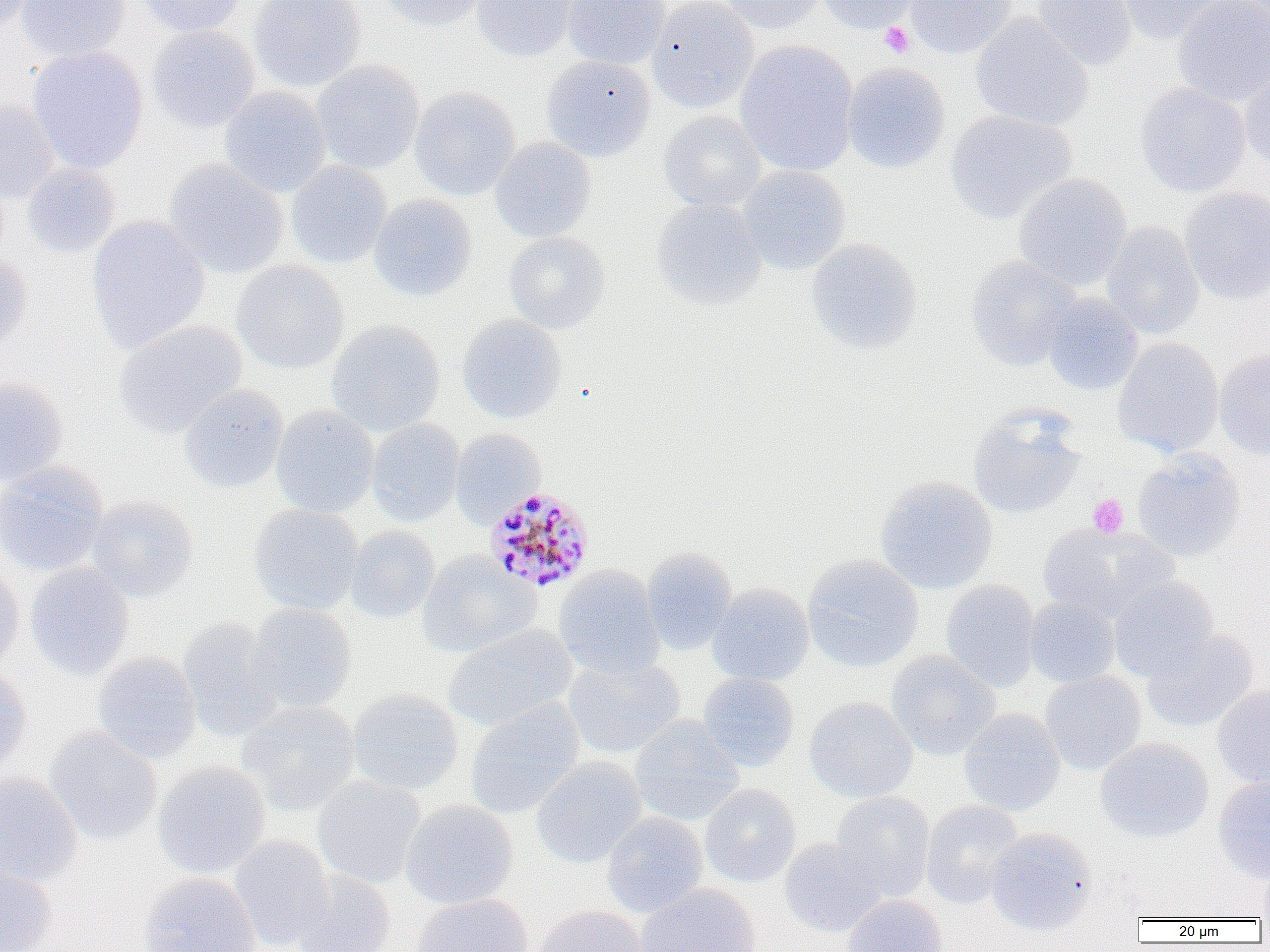
Summary:
  - Coordinate format: approximate bounding boxes as (x1,y1)-(x2,y2) corner pairs in pixels
  - Uninfected red blood cell locations: (0,0)-(34,33), (16,0)-(130,62), (133,0)-(247,37), (249,0)-(365,92), (375,0)-(487,31), (470,0)-(576,62), (562,0)-(669,70), (647,0)-(759,113), (716,0)-(826,33), (817,0)-(919,34), (905,0)-(1015,59), (1031,0)-(1136,72), (1116,0)-(1231,44), (1172,0)-(1270,105), (970,13)-(1093,132), (147,25)-(260,132), (734,40)-(858,176), (28,46)-(149,174), (542,55)-(656,162), (311,59)-(424,174), (1239,61)-(1270,170), (842,62)-(950,173), (1135,83)-(1251,198), (409,86)-(520,201), (219,87)-(331,197), (0,100)-(59,203), (945,110)-(1077,224), (658,111)-(766,212), (490,137)-(596,243), (164,159)-(289,278), (287,161)-(392,268), (22,164)-(119,258), (738,165)-(851,275), (1012,173)-(1132,291), (1179,186)-(1270,305), (369,194)-(478,303), (651,199)-(766,310), (86,215)-(209,354), (1101,222)-(1204,340), (504,232)-(610,334), (806,239)-(923,355), (0,249)-(32,355), (964,255)-(1082,372), (232,260)-(350,375), (1041,292)-(1144,395), (458,314)-(567,424), (113,320)-(248,438), (326,320)-(445,436), (1113,337)-(1224,458), (1213,348)-(1270,460), (0,377)-(68,486), (178,384)-(289,493), (271,406)-(379,518), (967,406)-(1086,520), (367,418)-(464,526), (450,429)-(547,526), (1132,448)-(1246,561), (0,461)-(108,577), (875,475)-(998,594), (86,495)-(199,602), (248,505)-(364,614), (1038,521)-(1173,622), (345,526)-(440,623), (641,547)-(738,655), (417,550)-(541,658), (802,553)-(923,673), (25,563)-(134,680), (0,565)-(24,675), (553,565)-(665,678), (1108,577)-(1219,680), (940,580)-(1040,693), (708,583)-(814,687), (1025,597)-(1120,688), (246,603)-(357,713), (177,616)-(285,742), (443,625)-(577,731), (1141,630)-(1258,733), (886,650)-(1001,760), (91,651)-(201,763), (562,655)-(684,760), (0,664)-(32,776), (1040,671)-(1146,774), (697,673)-(799,771), (1212,685)-(1270,788), (347,689)-(464,795), (804,696)-(917,803), (464,698)-(585,821), (236,700)-(361,815), (959,708)-(1065,816), (629,717)-(744,826), (44,726)-(163,846), (1095,737)-(1214,842), (530,755)-(648,868), (152,761)-(271,879), (0,772)-(83,886), (312,775)-(426,888), (1212,776)-(1270,883), (700,784)-(801,887), (830,792)-(935,901), (399,800)-(518,910), (921,800)-(1023,909), (602,812)-(708,918), (986,827)-(1096,935), (229,834)-(334,951), (779,837)-(887,937), (0,863)-(58,952), (1256,864)-(1270,922), (292,869)-(395,952), (138,872)-(261,952), (636,883)-(761,951), (411,893)-(534,952), (843,894)-(947,952), (533,905)-(648,952)
  - Platelet locations: (880,22)-(914,58), (1088,494)-(1129,538)
  - Plasmodium malariae-infected red blood cell locations: (483,486)-(596,594)
  - Slide-level diagnosis: Plasmodium malariae
  - Magnification: 1000x
  - Preparation: thin blood film
  - Image size: 1270×952 pixels
  - Field of view: one of a larger specimen
  - Modality: light microscopy